Outline each white blood cell.
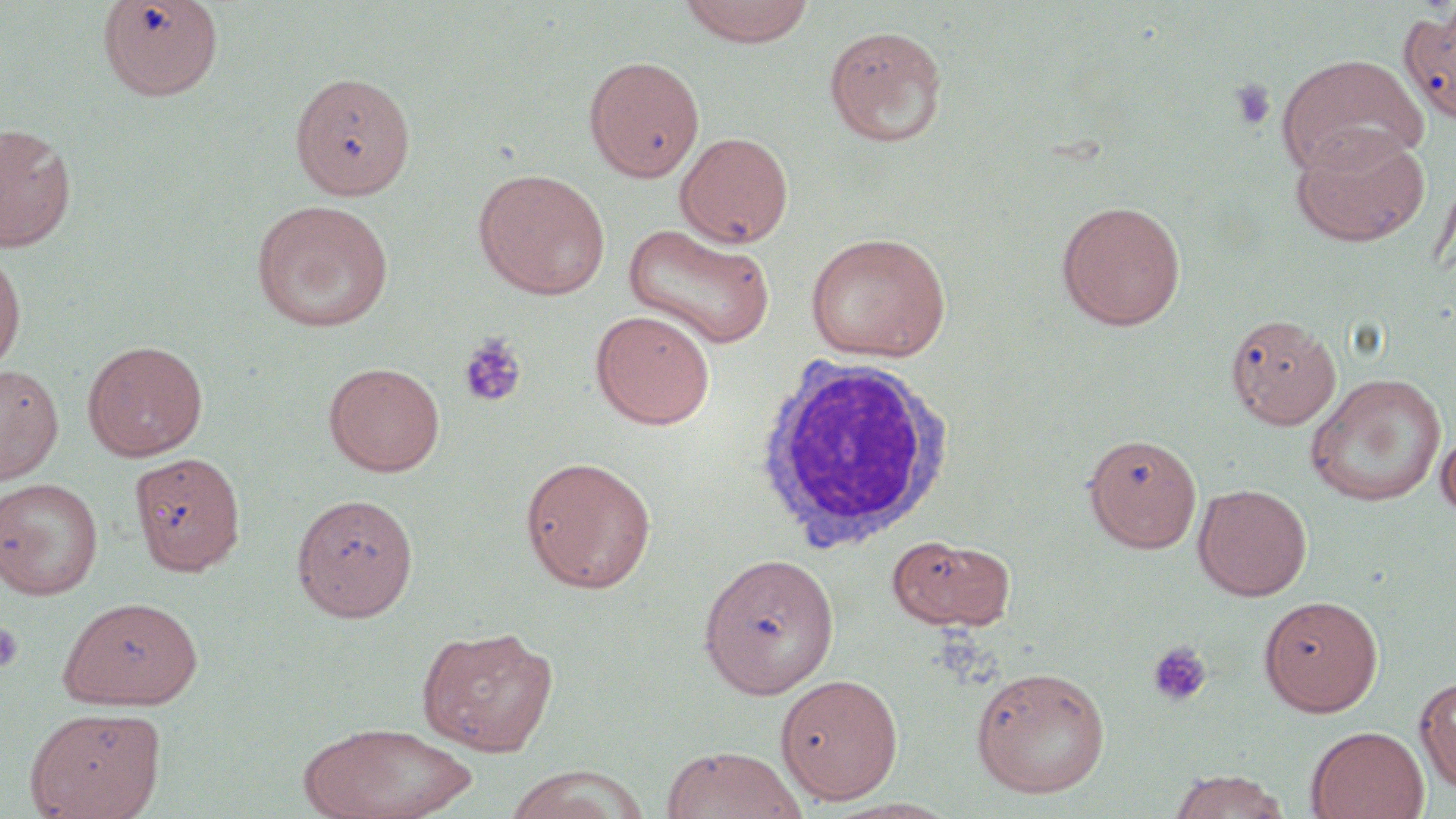

Approximate bounding boxes as (x1,y1)-(x2,y2) corner pairs in pixels.
White blood cells: (751,354)-(957,552).

Uninfected red blood cell locations: (96,0)-(225,101), (678,0)-(816,47), (1399,8)-(1456,125), (824,25)-(949,147), (1275,53)-(1429,176), (584,56)-(704,181), (0,122)-(77,252), (1289,126)-(1430,248), (675,131)-(794,248), (472,167)-(611,300), (250,198)-(395,333), (1056,200)-(1187,331), (623,222)-(776,350), (804,231)-(952,362), (0,247)-(26,374), (590,309)-(715,429), (1225,312)-(1343,430), (82,339)-(208,461), (323,361)-(446,477), (0,363)-(63,483), (1304,373)-(1447,507), (1437,424)-(1456,524), (1083,431)-(1202,552), (128,452)-(247,575), (519,455)-(657,594), (0,477)-(104,599), (1193,483)-(1312,601), (291,493)-(419,620), (886,533)-(1017,632), (698,552)-(840,698), (1258,595)-(1384,716), (58,596)-(203,709), (416,624)-(558,756), (970,665)-(1111,798), (776,673)-(903,803), (1415,675)-(1456,793), (25,706)-(165,818), (298,720)-(480,819), (1306,725)-(1429,819), (660,745)-(809,819), (503,767)-(647,819), (1166,769)-(1291,818). Platelet locations: (1229,77)-(1277,132), (458,332)-(528,409), (0,620)-(24,673), (1146,642)-(1213,708). Slide-level diagnosis: negative for blood parasites. Single field of view. 1000x magnification. Light microscopy. Thin blood film. May-Grünwald-Giemsa-stained preparation. Image is 1456×819 pixels.